Identify the blood parasite species.
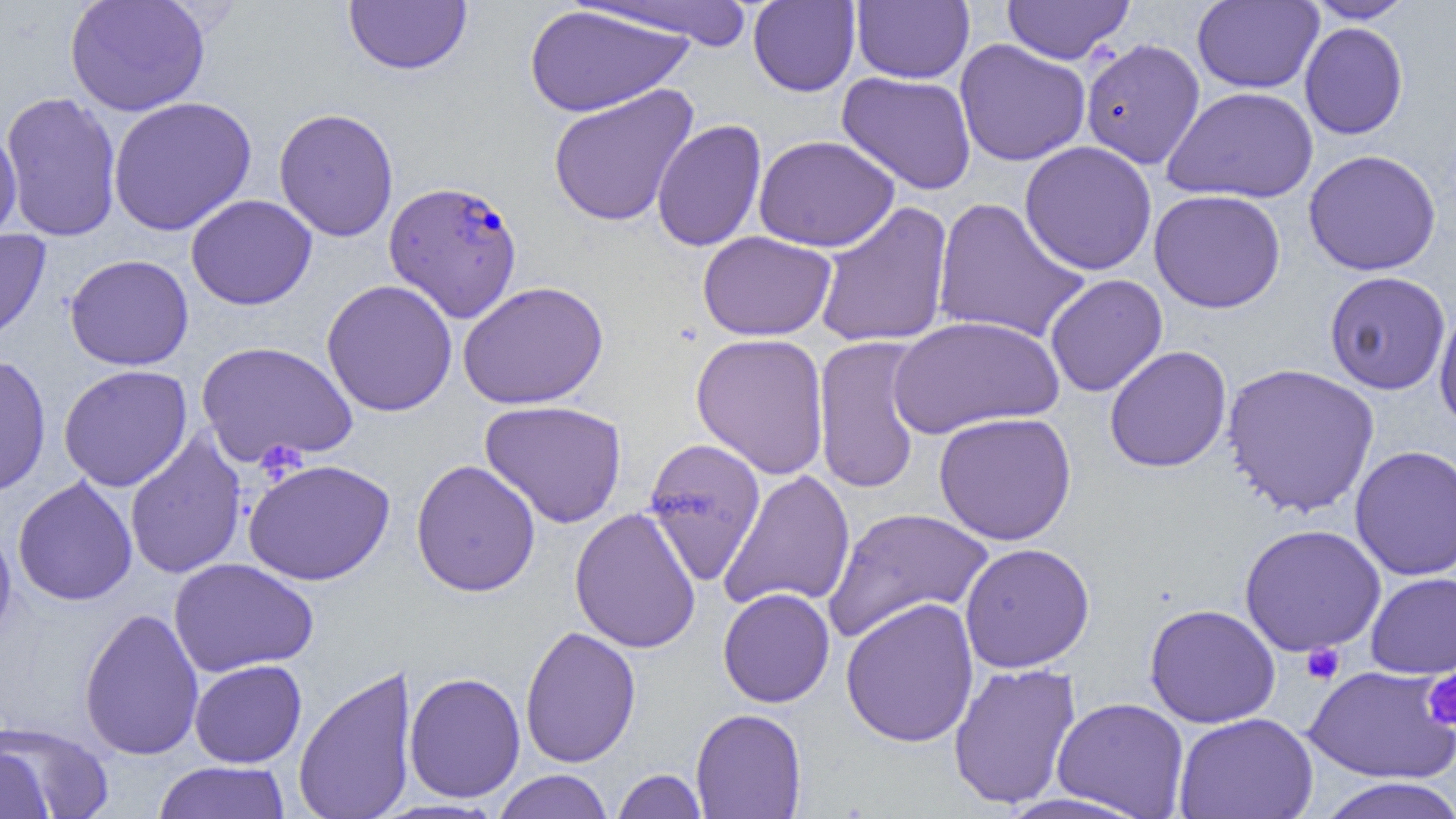
Plasmodium falciparum.

preparation = thin blood smear
field of view = one of a larger specimen
platelet locations = approximate bounding boxes as (x1, y1, x2, y2) in pixels: (1301, 643, 1344, 685), (1422, 669, 1456, 731)
Plasmodium falciparum-infected red blood cell locations = approximate bounding boxes as (x1, y1, x2, y2) in pixels: (383, 179, 523, 322)
modality = light microscopy
uninfected red blood cell locations = approximate bounding boxes as (x1, y1, x2, y2) in pixels: (66, 0, 210, 117), (343, 0, 472, 75), (851, 0, 974, 84), (1002, 0, 1134, 64), (1305, 0, 1417, 23), (576, 1, 761, 48), (748, 1, 861, 97), (1192, 1, 1324, 93), (524, 5, 693, 117), (1299, 21, 1408, 140), (954, 38, 1091, 167), (1080, 38, 1206, 169), (837, 71, 977, 195), (547, 83, 699, 227), (1162, 86, 1318, 204), (1, 91, 123, 242), (108, 96, 257, 236), (273, 108, 399, 242), (651, 119, 767, 252), (0, 123, 22, 247), (754, 134, 900, 252), (1019, 141, 1157, 275), (1303, 149, 1441, 276), (1149, 189, 1286, 313), (185, 194, 317, 310), (931, 196, 1090, 345), (813, 201, 954, 349), (0, 228, 52, 346), (697, 230, 837, 341), (64, 254, 194, 371), (1324, 271, 1451, 395), (1044, 274, 1168, 397), (321, 278, 458, 417), (458, 280, 609, 410), (1434, 304, 1456, 435), (887, 315, 1063, 439), (691, 332, 831, 480), (812, 335, 927, 495), (196, 340, 359, 467), (1104, 345, 1232, 473), (0, 354, 51, 498), (1221, 363, 1380, 518), (58, 364, 193, 491), (479, 399, 628, 528), (933, 411, 1077, 546), (124, 432, 247, 579), (642, 437, 767, 585), (1350, 445, 1456, 580), (243, 458, 395, 586), (410, 459, 541, 597), (719, 470, 856, 612), (13, 476, 138, 606), (569, 506, 701, 654), (822, 507, 994, 643), (0, 517, 17, 650), (1239, 523, 1386, 657), (959, 542, 1095, 673), (168, 557, 318, 676), (1365, 572, 1456, 678), (717, 588, 835, 708), (840, 597, 979, 747), (1144, 603, 1281, 728), (79, 606, 204, 761), (519, 625, 641, 768), (190, 659, 307, 768), (947, 662, 1082, 809), (293, 663, 418, 819), (1304, 664, 1456, 784), (404, 671, 526, 803), (1051, 697, 1189, 818), (691, 708, 807, 819), (1174, 712, 1319, 819), (0, 719, 114, 819), (0, 744, 56, 819), (152, 760, 290, 818), (612, 768, 707, 818), (492, 770, 614, 819), (1314, 777, 1456, 819)
magnification = 1000x
image size = 1456×819 pixels